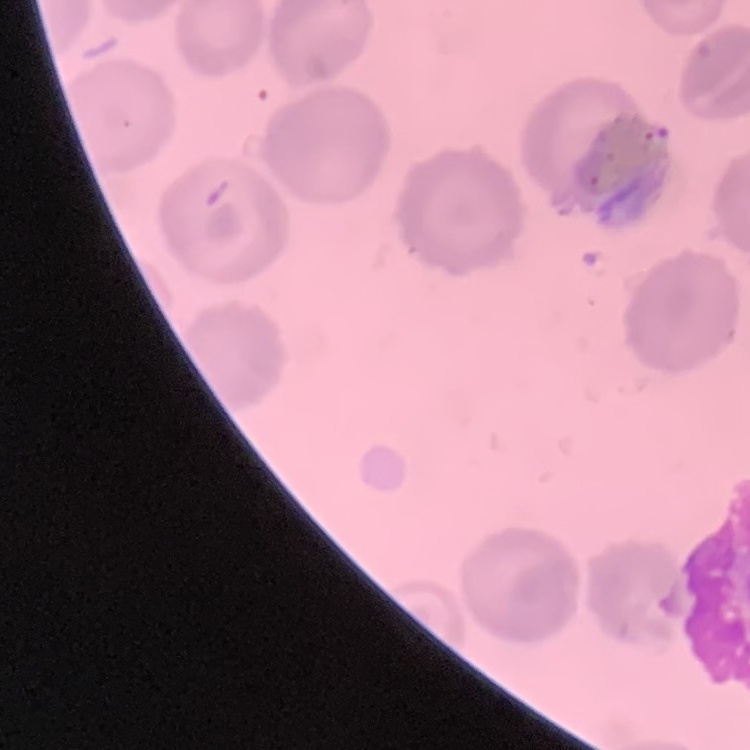

The red blood cells exhibit no rouleaux formation. Field's or Giemsa stain. Thin blood film. Square crop of a larger photomicrograph.